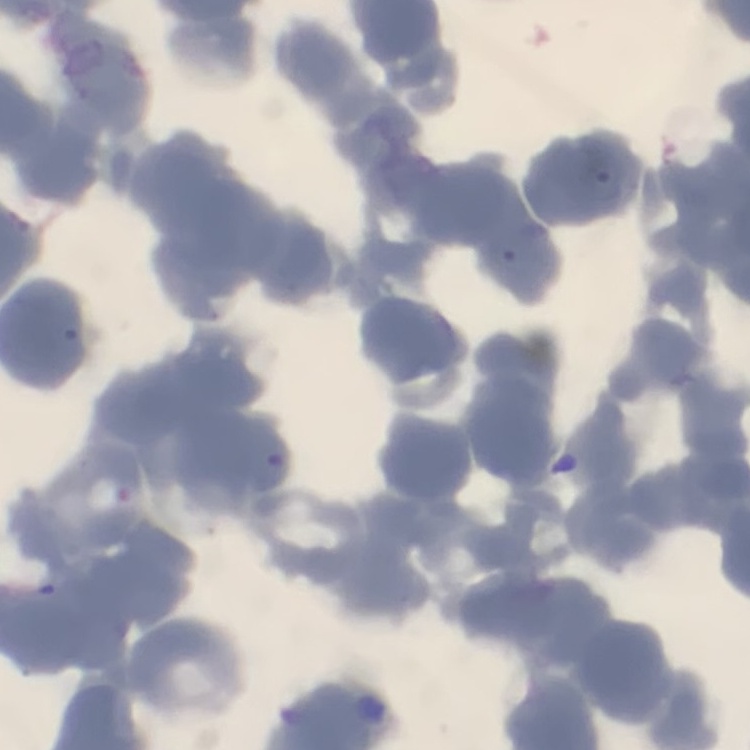

red blood cell morphology = rouleaux formation
stain = Field's or Giemsa
image type = one tile cut from a larger photomicrograph
preparation = thin blood film